Assess for malaria.
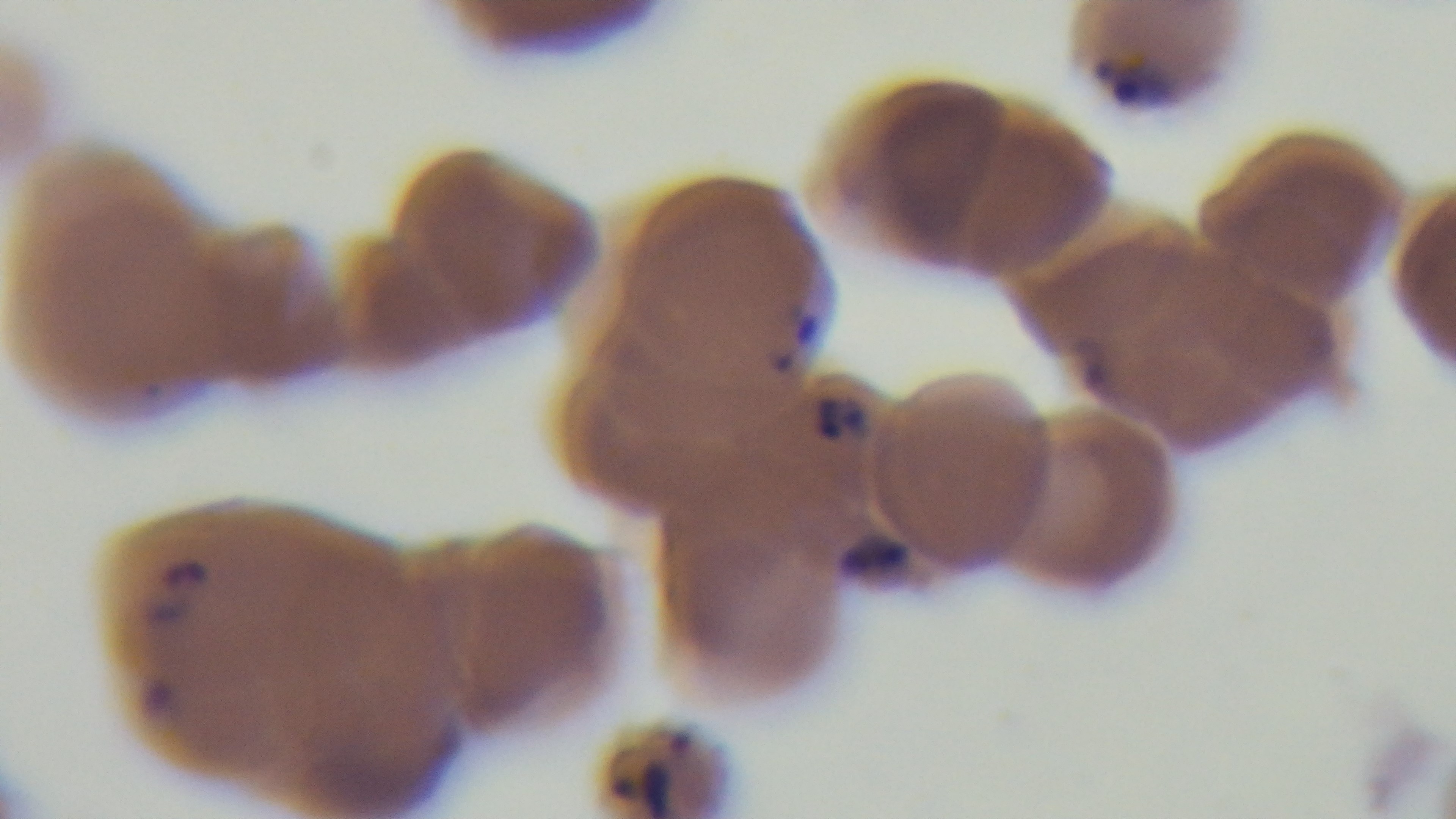
Positive.

Preparation: thin. Oil-immersion objective, 100x. Photomicrograph. Mounted 4K digital camera. Giemsa-stained. Single field of view.